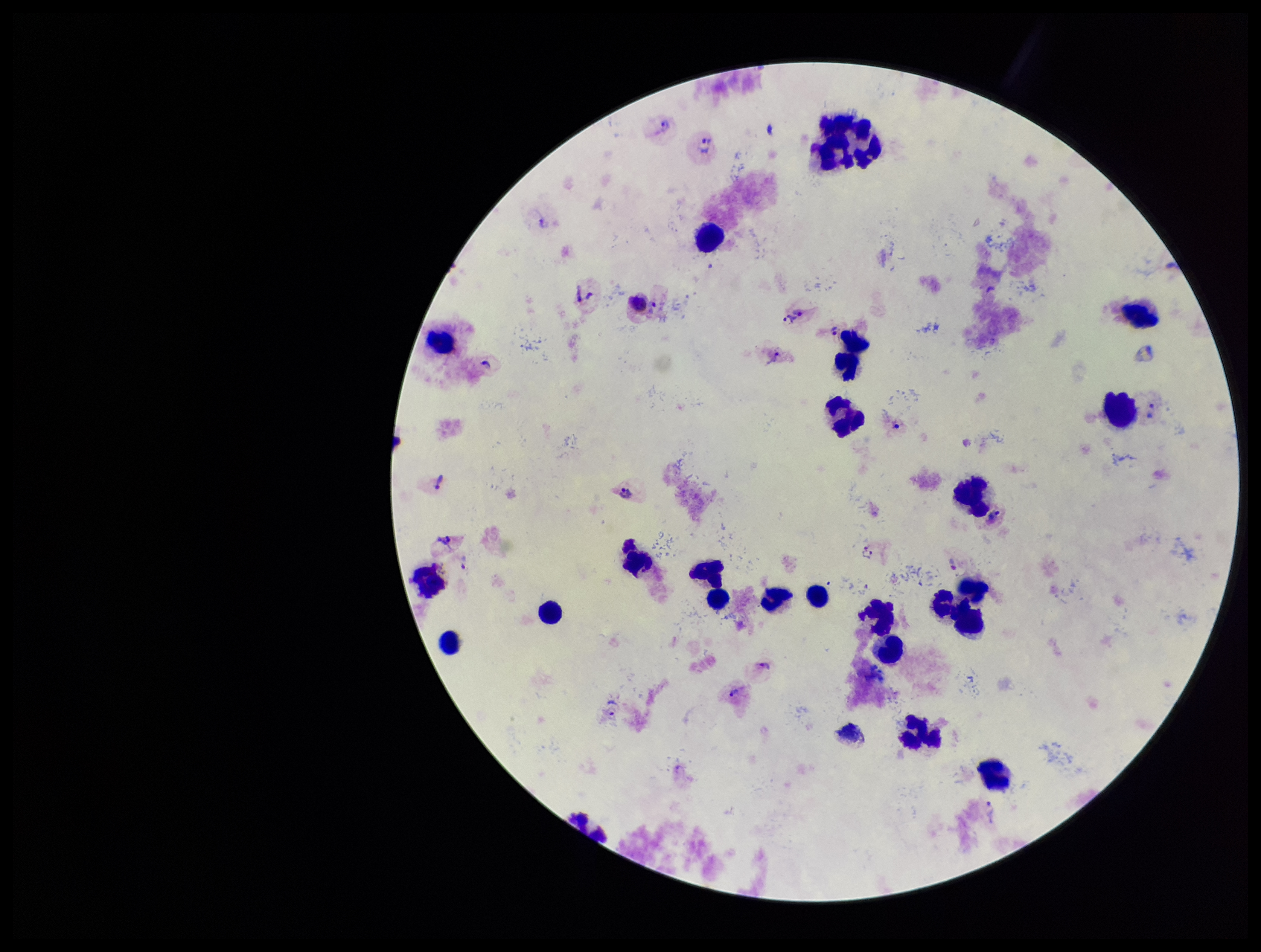
Image is 1261×952 pixels. Patient malaria status: infected. Species reported for this patient: Plasmodium vivax. Photographed through the microscope eyepiece with a smartphone camera. Preparation: thick smear. Single field of view. Giemsa stain. Plasmodium parasites: seen. Leukocyte count: 23. Parasite count: 24.